Give the position of every Plasmodium parasite visible.
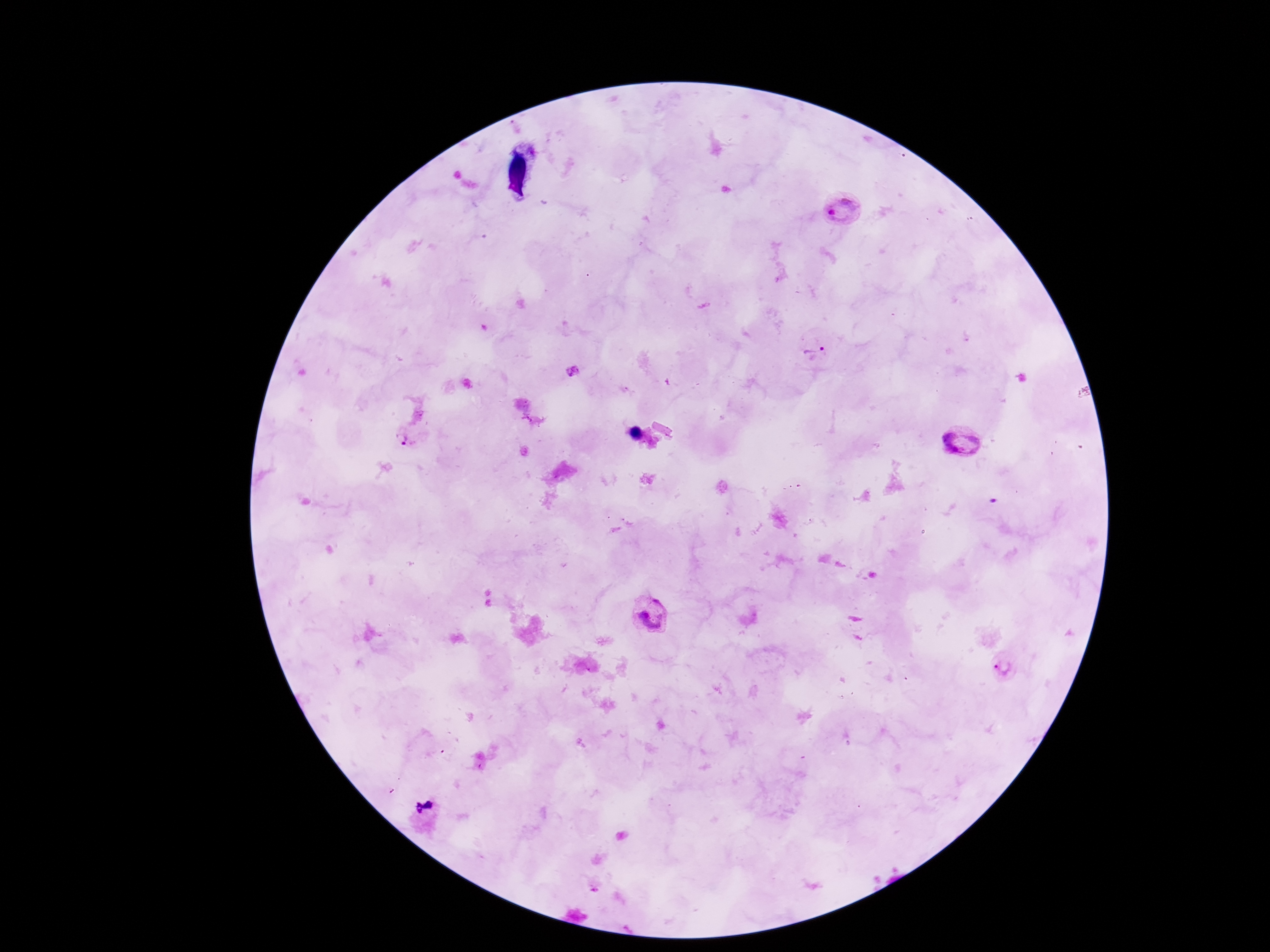

Approximate object centers, in pixels from the top-left corner.
Plasmodium parasites: (x=845, y=211), (x=816, y=353), (x=573, y=371), (x=410, y=438), (x=963, y=444), (x=648, y=615), (x=1001, y=667).

Single field of view. Patient malaria status: positive. 100x magnification. Thick blood smear. Image is 1270×952 pixels. Photographed through the microscope eyepiece with a smartphone camera. Giemsa-stained preparation.